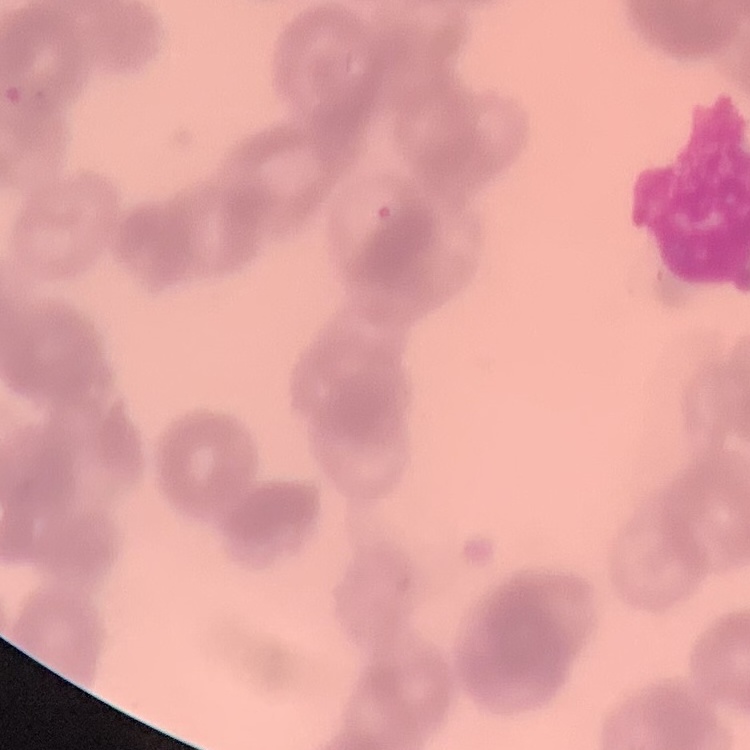
Summary:
  - Red blood cell morphology: rouleaux formation
  - Stain: Field's or Giemsa
  - Image type: one tile cut from a larger photomicrograph
  - Preparation: thin peripheral smear